Identify the cell.
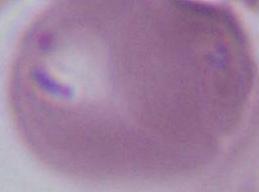

This is an erythrocyte.

Summary:
  - Magnification: 1000x
  - Modality: photomicrograph